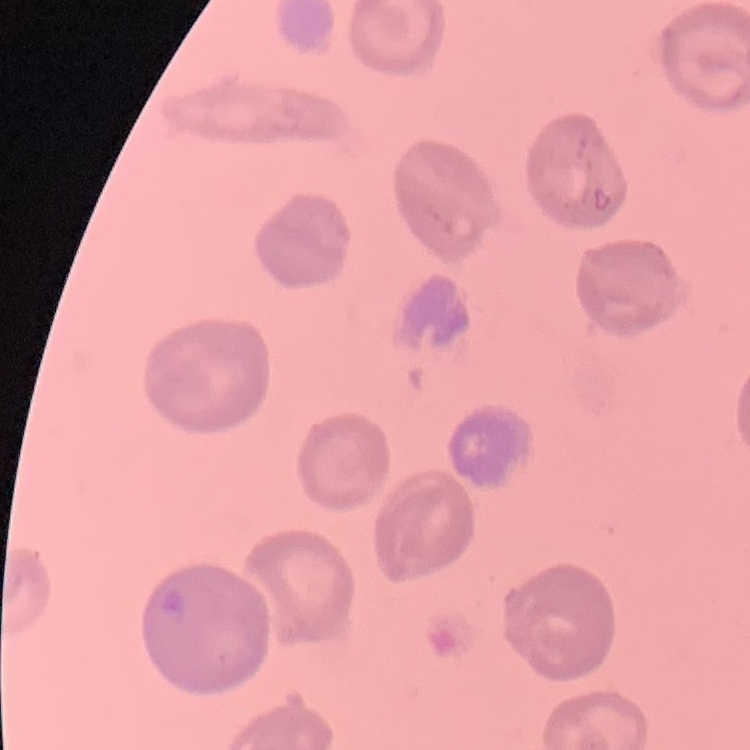

The red blood cells exhibit no rouleaux formation. Field's or Giemsa stain. Square crop of a larger photomicrograph. Thin blood film.